Give the extent of all Plasmodium falciparum-infected red blood cells.
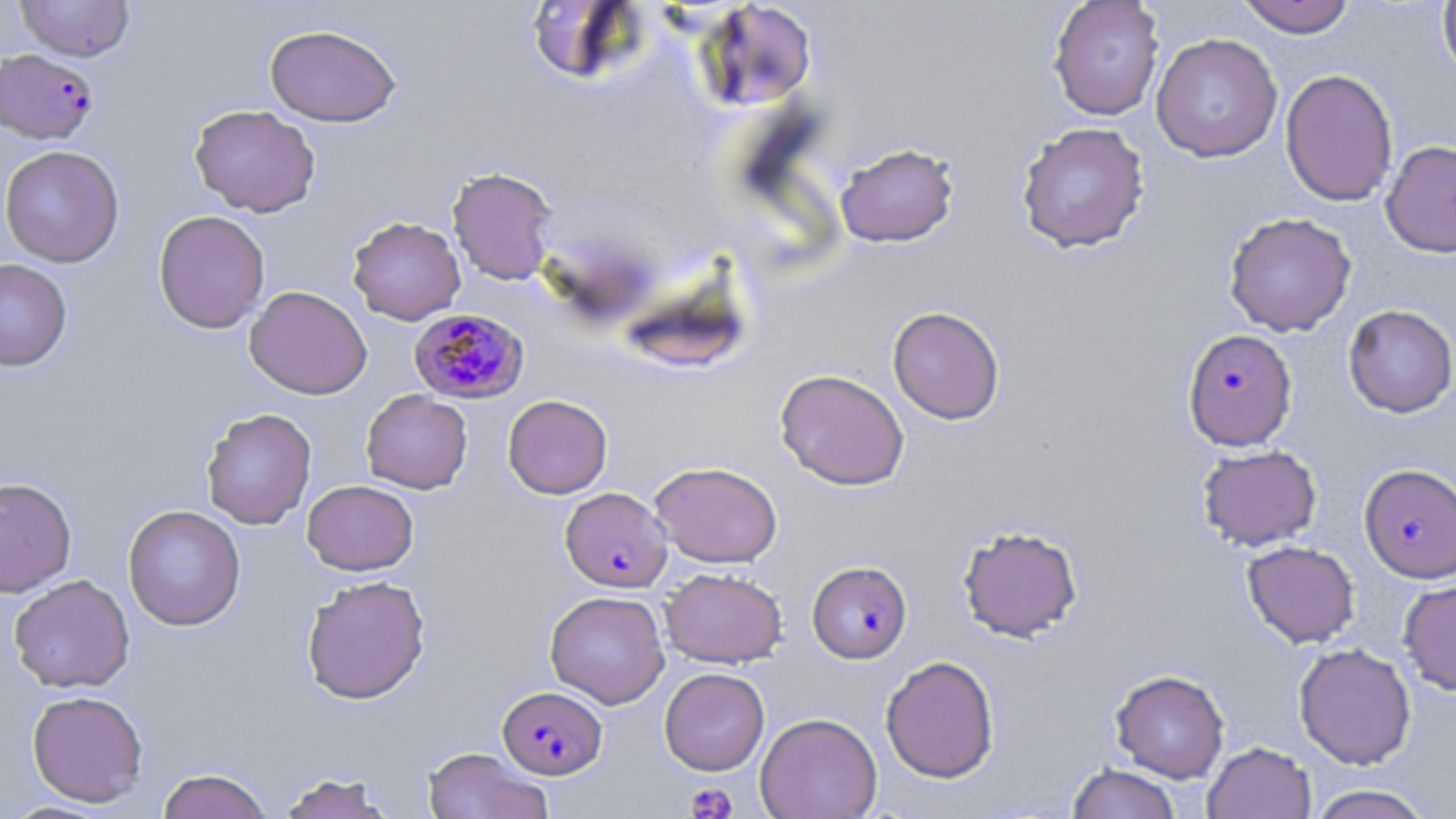

Approximate bounding boxes as named x1/y1/x2/y2 corners in pixels.
Plasmodium falciparum-infected red blood cells: (x1=0, y1=48, x2=99, y2=144), (x1=409, y1=308, x2=529, y2=405), (x1=1182, y1=329, x2=1298, y2=450), (x1=1359, y1=464, x2=1456, y2=582), (x1=560, y1=487, x2=672, y2=592), (x1=807, y1=560, x2=912, y2=663), (x1=498, y1=686, x2=606, y2=779).

{
  "slide_level_diagnosis": "Plasmodium falciparum",
  "platelet_locations": "approximate bounding boxes as named x1/y1/x2/y2 corners in pixels: (x1=684, y1=783, x2=737, y2=819)",
  "stain": "May-Grünwald-Giemsa",
  "preparation": "thin blood film",
  "field_of_view": "one of a larger specimen",
  "image_size": "1456×819 pixels",
  "uninfected_red_blood_cell_locations": "approximate bounding boxes as named x1/y1/x2/y2 corners in pixels: (x1=15, y1=0, x2=135, y2=62), (x1=1047, y1=0, x2=1165, y2=120), (x1=1234, y1=0, x2=1357, y2=38), (x1=698, y1=1, x2=818, y2=112), (x1=1437, y1=1, x2=1456, y2=86), (x1=264, y1=23, x2=401, y2=127), (x1=1150, y1=33, x2=1283, y2=162), (x1=1280, y1=68, x2=1398, y2=207), (x1=189, y1=104, x2=320, y2=217), (x1=1016, y1=122, x2=1150, y2=253), (x1=1380, y1=140, x2=1456, y2=257), (x1=835, y1=142, x2=960, y2=248), (x1=0, y1=145, x2=124, y2=267), (x1=446, y1=166, x2=559, y2=285), (x1=153, y1=210, x2=270, y2=334), (x1=1223, y1=212, x2=1357, y2=336), (x1=347, y1=216, x2=466, y2=325), (x1=0, y1=259, x2=72, y2=371), (x1=245, y1=285, x2=372, y2=399), (x1=1343, y1=304, x2=1456, y2=418), (x1=887, y1=306, x2=1005, y2=425), (x1=774, y1=368, x2=910, y2=490), (x1=361, y1=389, x2=472, y2=494), (x1=503, y1=394, x2=613, y2=499), (x1=201, y1=407, x2=316, y2=530), (x1=1197, y1=444, x2=1322, y2=550), (x1=650, y1=461, x2=783, y2=567), (x1=1, y1=476, x2=77, y2=597), (x1=302, y1=480, x2=419, y2=576), (x1=123, y1=504, x2=246, y2=631), (x1=957, y1=524, x2=1084, y2=642), (x1=1242, y1=541, x2=1360, y2=648), (x1=660, y1=566, x2=788, y2=668), (x1=8, y1=574, x2=135, y2=693), (x1=301, y1=574, x2=431, y2=705), (x1=1398, y1=578, x2=1456, y2=696), (x1=545, y1=590, x2=670, y2=708), (x1=1293, y1=643, x2=1416, y2=769), (x1=880, y1=655, x2=1000, y2=783), (x1=659, y1=668, x2=770, y2=775), (x1=1110, y1=669, x2=1229, y2=783), (x1=27, y1=690, x2=149, y2=807), (x1=755, y1=712, x2=882, y2=819), (x1=1203, y1=741, x2=1316, y2=819), (x1=422, y1=746, x2=553, y2=819), (x1=1066, y1=763, x2=1182, y2=819), (x1=156, y1=768, x2=274, y2=818), (x1=275, y1=771, x2=398, y2=819), (x1=1306, y1=784, x2=1435, y2=819), (x1=4, y1=800, x2=115, y2=818)",
  "magnification": "1000x",
  "modality": "light microscopy"
}